Assess this cell for malaria.
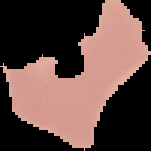

Uninfected.

Summary:
  - Image type: segmented cell region on a black background
  - Image size: 151×151 pixels
  - Preparation: thin blood smear